Draw a bounding box around every Plasmodium parasite, every leukocyte, and every artifact (stain precipitate or debris).
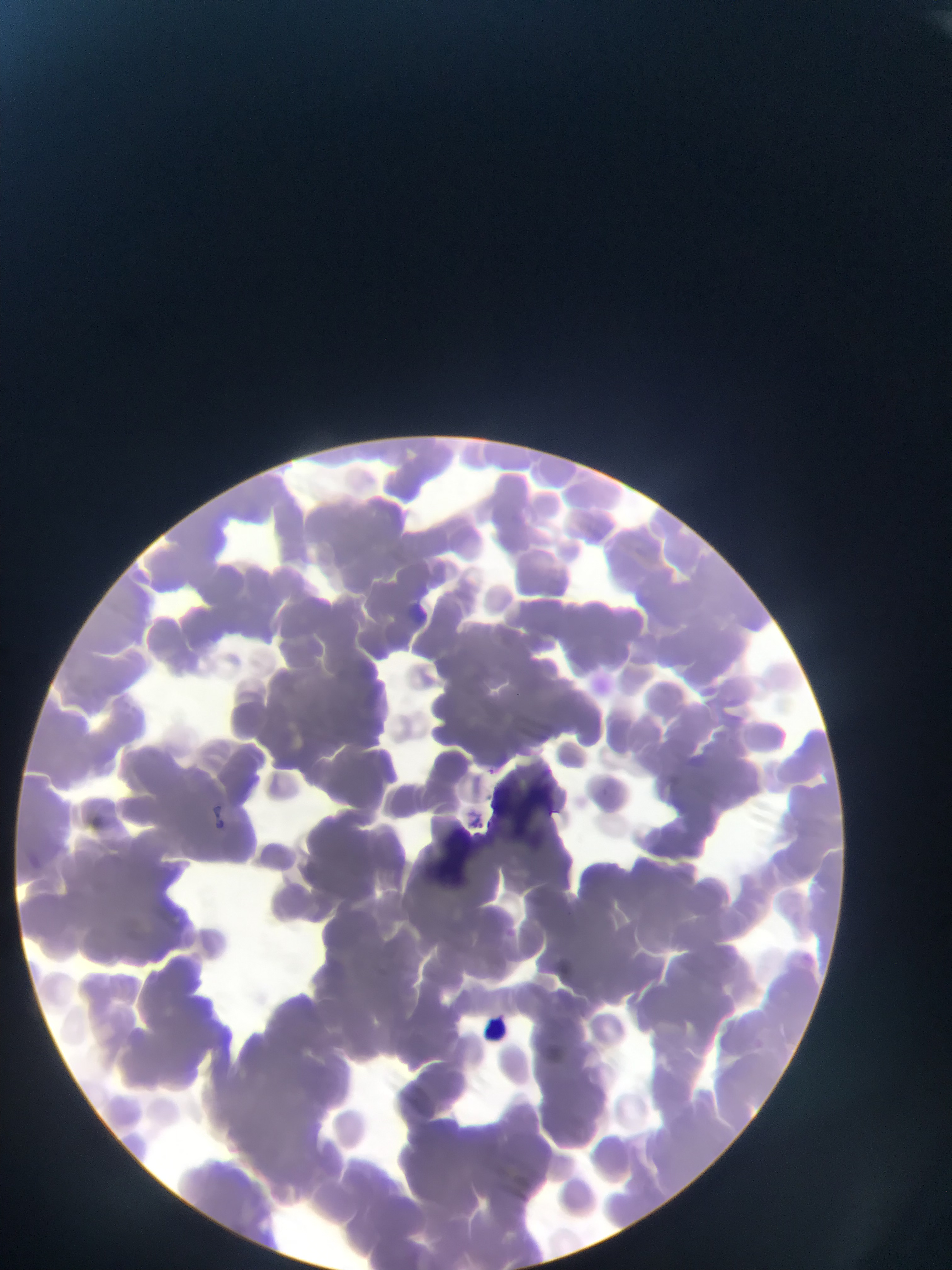

Approximate bounding boxes as (left, top, right, bottom) in pixels.
No Plasmodium parasites observed.
No leukocytes observed.
Artifacts (stain precipitate or debris): (486, 772, 563, 834), (419, 822, 485, 885).

image size = 952×1270 pixels
preparation = thin blood smear
capture = mobile-phone photograph through a microscope
country = Ghana
field of view = single